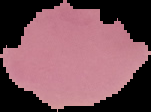

Summary:
  - Result: no malaria parasites detected
  - Image type: cell region segmented out of the field of view; surrounding area masked to black
  - Preparation: thin blood film
  - Image size: 151×112 pixels